Name the parasite shown.
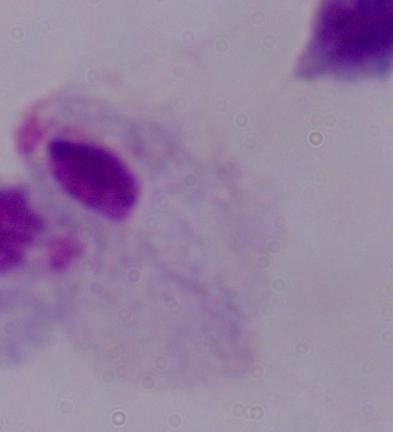

A trichomonad.

Captured at 1000x magnification. Micrograph.